Assess this cell for malaria.
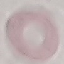

Uninfected.

Summary:
  - Stain: Giemsa
  - Image type: automatically extracted cell patch, resized to 64 × 64 pixels
  - Preparation: thin smear
  - Capture: smartphone through the microscope eyepiece